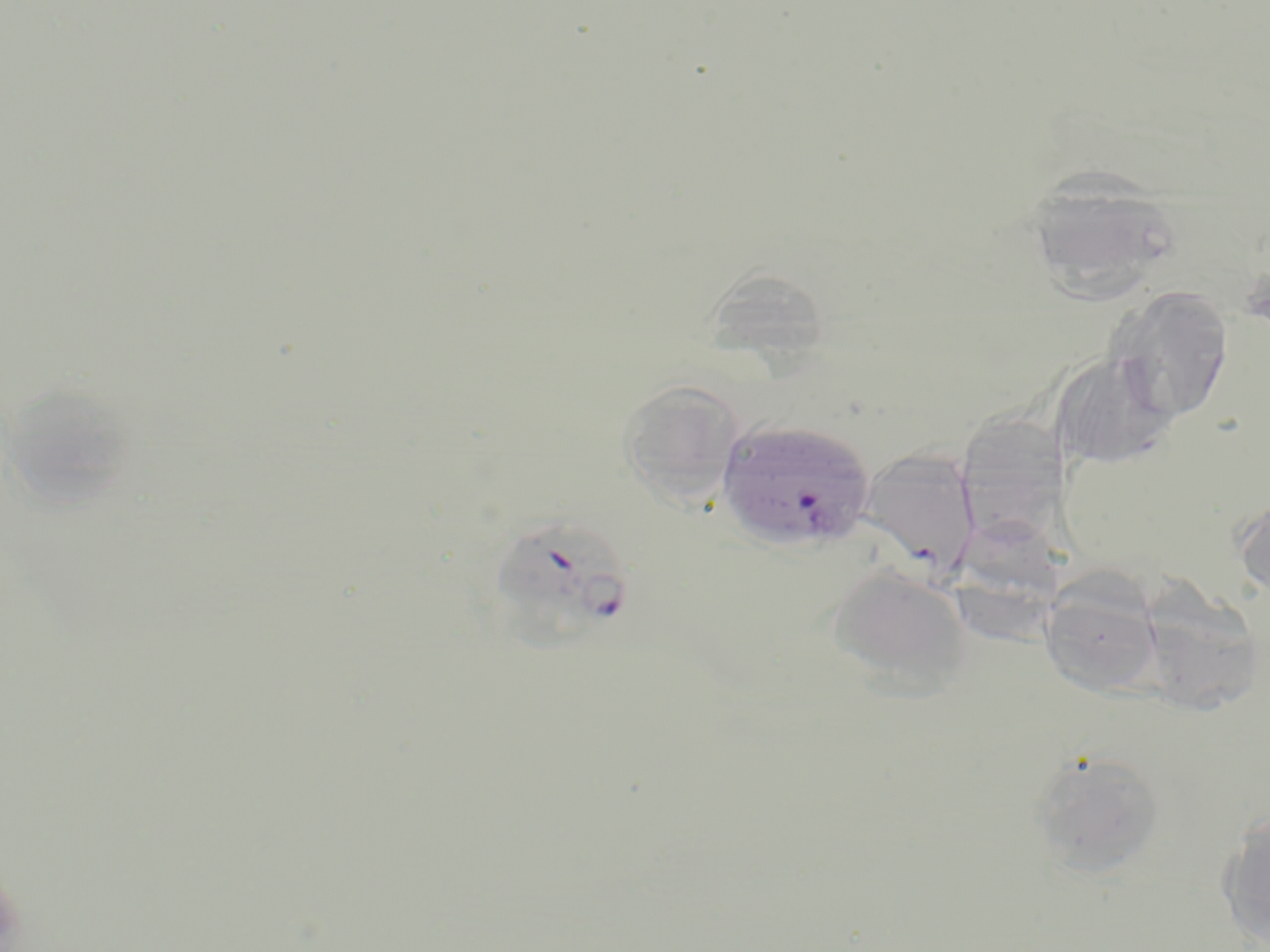
Summary:
  - Coordinate format: approximate bounding boxes as [x1, y1, x2, y2] in pixels
  - Plasmodium falciparum-infected red blood cell locations: [715, 417, 876, 553], [488, 514, 635, 645]
  - Uninfected red blood cell locations: [1024, 168, 1183, 301], [709, 277, 826, 381], [1108, 286, 1234, 426], [1052, 352, 1176, 471], [9, 369, 144, 529], [618, 379, 745, 508], [968, 411, 1066, 554], [860, 448, 981, 581], [1233, 495, 1270, 601], [950, 520, 1065, 651], [826, 562, 974, 696], [1138, 565, 1261, 720], [1039, 578, 1164, 698], [1027, 747, 1168, 879], [1218, 809, 1270, 947]
  - Slide-level diagnosis: Plasmodium falciparum
  - Stain: May-Grünwald-Giemsa
  - Image size: 1270×952 pixels
  - Modality: optical microscopy
  - Magnification: 1000x
  - Preparation: thin blood film
  - Field of view: one of a larger specimen